Assess this cell for malaria.
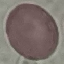
Uninfected.

Summary:
  - Stain: Giemsa
  - Preparation: thin smear
  - Capture: smartphone through the microscope eyepiece
  - Image type: cell patch, automatically extracted from a larger field of view and resized to 64 × 64 pixels